Assess this cell for malaria.
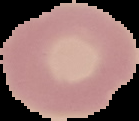

Uninfected.

image_size: 139×121 pixels
preparation: thin blood smear
image_type: segmented cell region with the area outside set to black